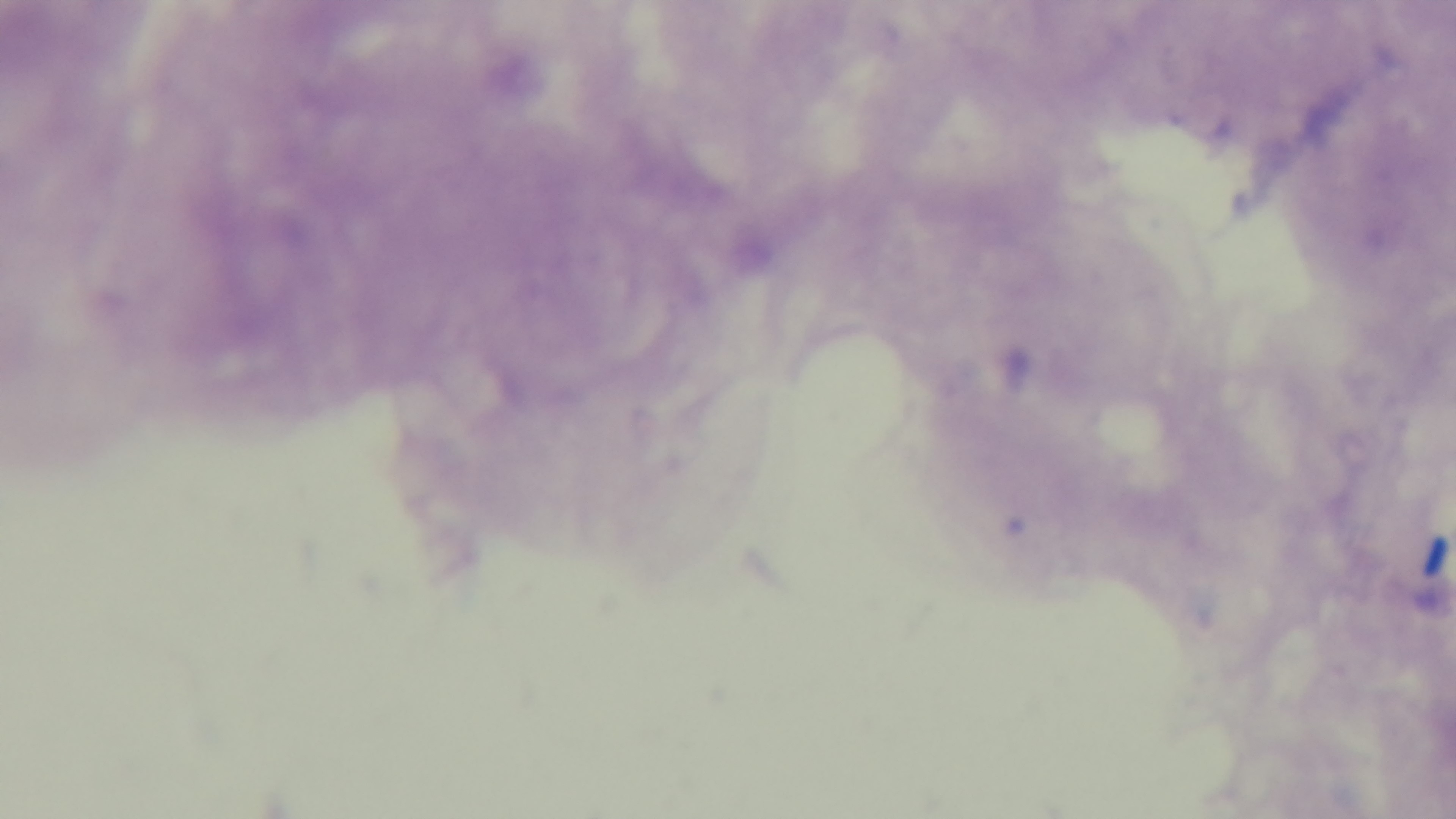
Summary:
  - Field of view: single
  - Modality: light microscopy
  - Preparation: thick smear
  - Capture: mounted 4K digital camera
  - Stain: Giemsa
  - Malaria status: uninfected
  - Objective: 100x oil immersion